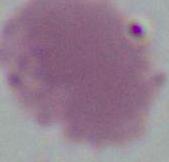
Summary:
  - Identification: erythrocyte
  - Modality: photomicrograph
  - Magnification: 1000x